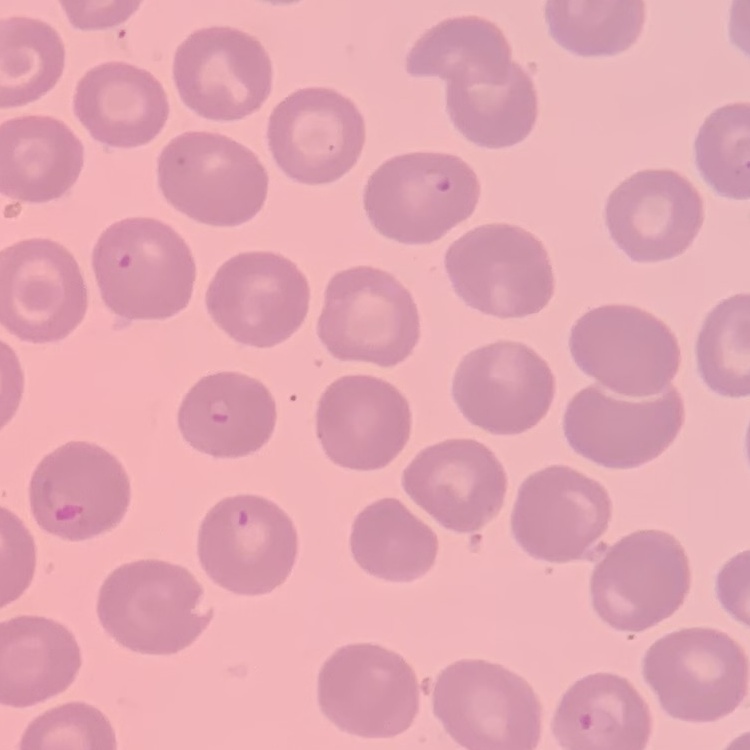
{
  "red_blood_cell_morphology": "no rouleaux formation",
  "preparation": "thin blood film",
  "image_type": "square crop of a larger photomicrograph",
  "stain": "Field's or Giemsa"
}